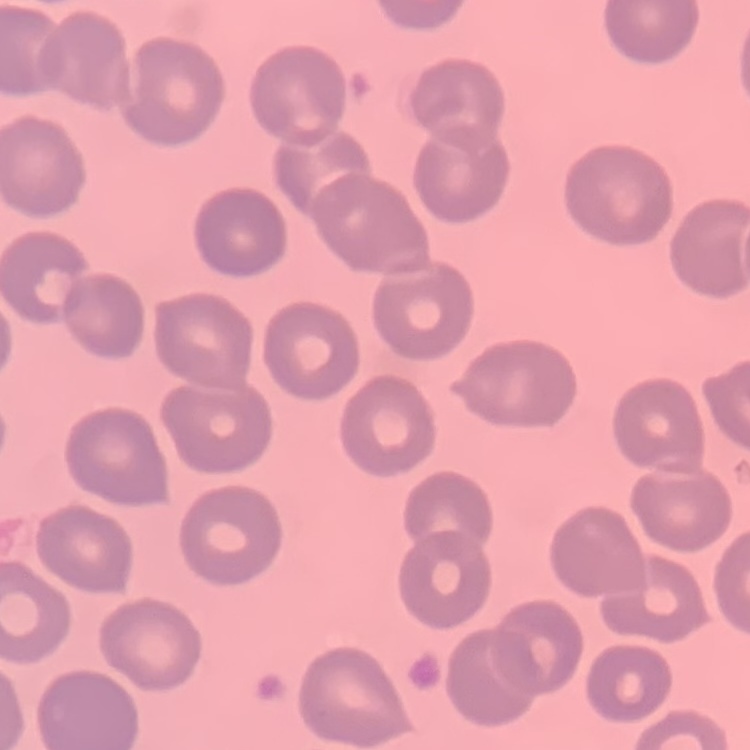

Summary:
  - Erythrocyte morphology: no rouleaux formation
  - Stain: Field's or Giemsa
  - Preparation: thin blood film
  - Image type: one tile cut from a larger photomicrograph